Report the malaria status of this cell.
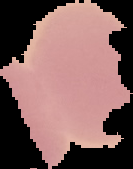

It is uninfected.

{
  "preparation": "thin blood smear",
  "image_size": "133×169 pixels",
  "image_type": "cell region segmented out of the field of view; surrounding area masked to black"
}